Assess the background quality.
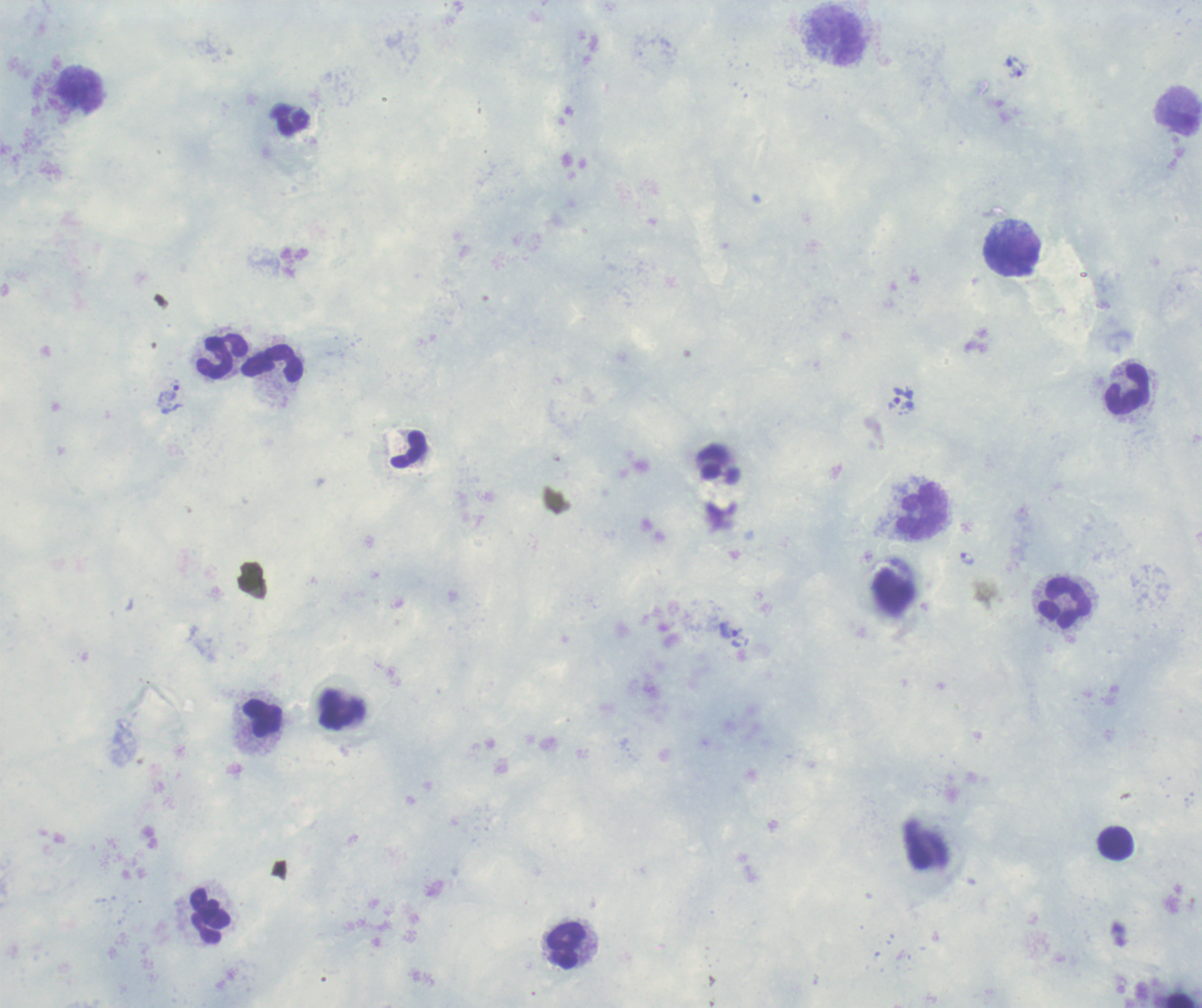
It is poor.

Approximate centers as (x, y) in pixels. Leukocyte locations: (837, 36), (80, 89), (1178, 119), (1011, 252), (220, 355), (273, 363), (1126, 390), (923, 510), (1064, 604), (263, 719), (1115, 843), (210, 915), (566, 946). Trophozoite locations: (1018, 69), (170, 393), (904, 405), (966, 558), (729, 630). Coloration quality: good. Thick blood smear. Image is 1202×1008 pixels. Single field of view. Captured at 100x magnification. Romanowsky stain. Result: positive for Plasmodium parasites. Previously used in a real diagnosis.